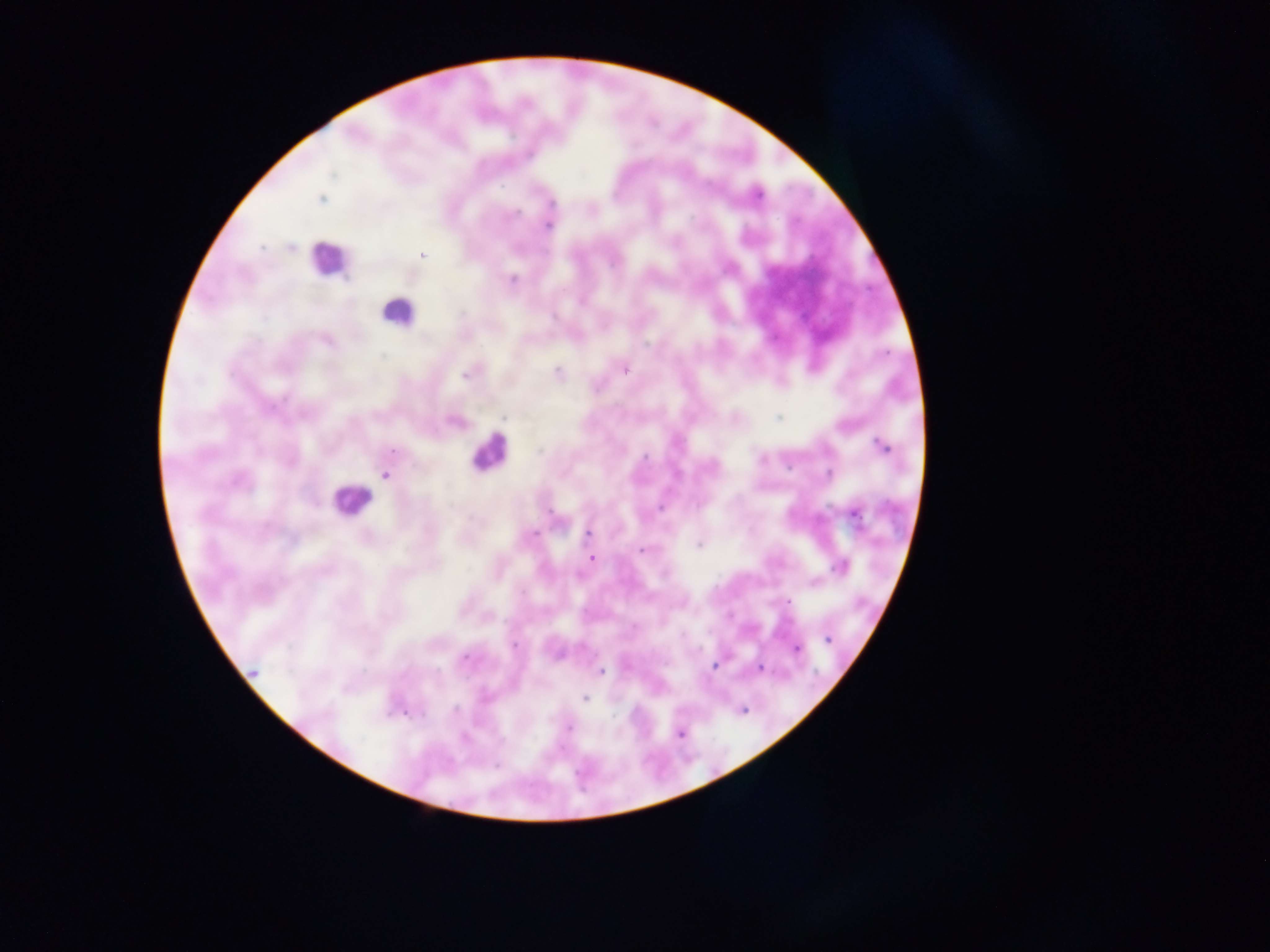
Approximate centers as {x, y} in pixels. Leukocyte locations: {328, 259}, {397, 312}, {488, 451}, {351, 500}. Plasmodium parasite locations: {756, 194}, {321, 198}, {548, 224}, {422, 255}, {510, 280}, {624, 368}, {470, 371}, {558, 373}, {503, 416}, {779, 416}, {455, 421}, {882, 446}, {829, 473}, {385, 475}, {854, 512}, {588, 534}, {700, 543}, {642, 549}, {592, 558}, {841, 566}, {813, 583}, {828, 638}, {795, 648}, {716, 665}, {760, 668}, {600, 672}, {252, 673}, {584, 698}, {742, 709}, {404, 711}, {568, 726}, {680, 733}. Photographed through a microscope with a mobile-phone camera. Thick blood film. Collected in Ghana. Image is 1270×952 pixels. One field of view.